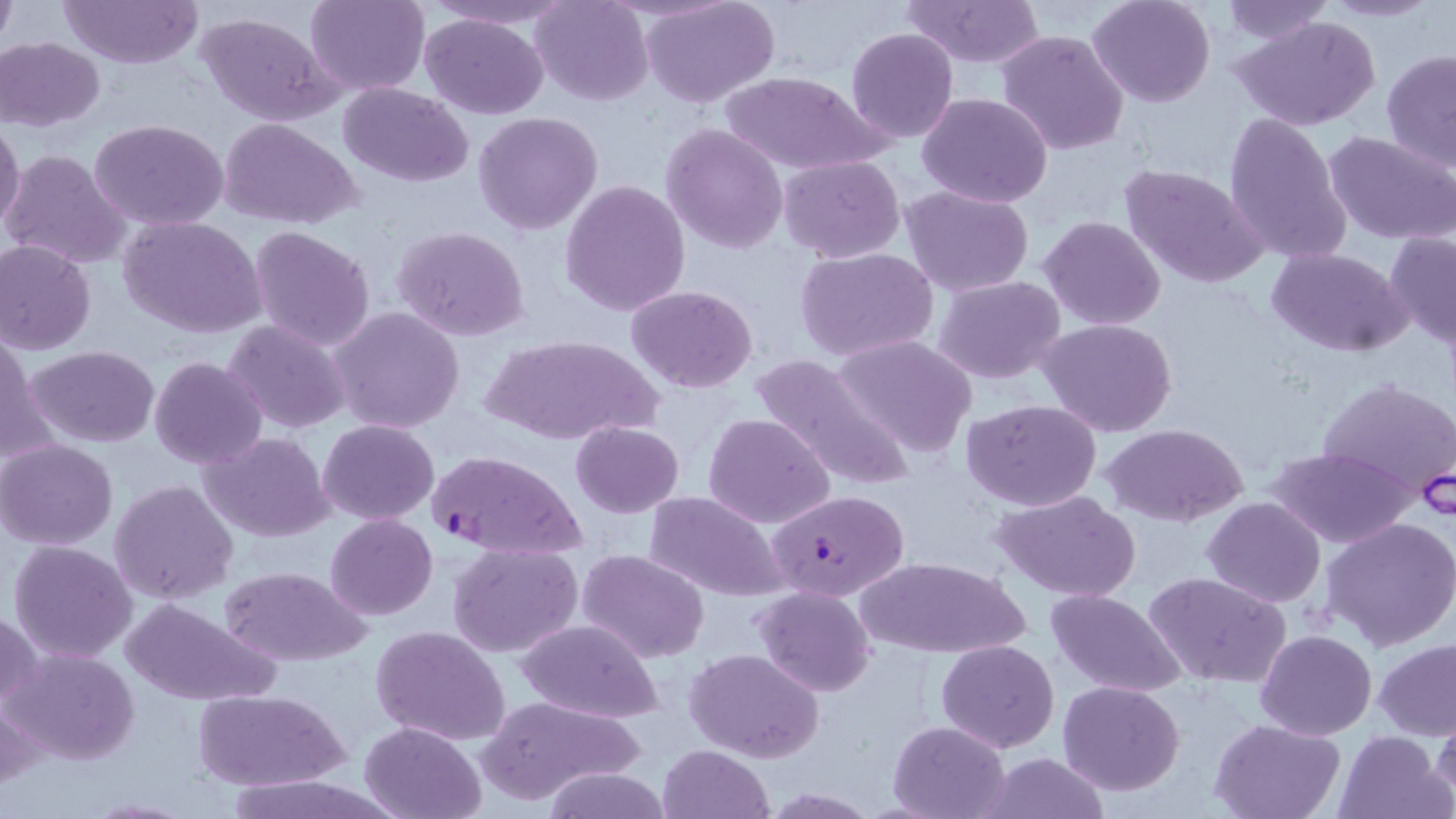 Approximate bounding boxes as (x1,y1)-(x2,y2) corner pairs in pixels. Plasmodium falciparum-infected red blood cell locations: (427,451)-(586,562), (767,487)-(907,604). Uninfected red blood cell locations: (58,0)-(203,70), (306,0)-(430,96), (427,0)-(572,29), (528,0)-(652,107), (645,0)-(780,107), (902,0)-(1045,67), (1087,0)-(1217,108), (1314,0)-(1444,22), (1222,1)-(1333,43), (1,5)-(17,53), (197,12)-(342,127), (418,13)-(550,120), (1236,16)-(1381,132), (846,28)-(960,145), (996,30)-(1128,155), (1,37)-(104,129), (1382,48)-(1456,174), (716,68)-(891,175), (340,82)-(474,185), (918,93)-(1053,208), (1224,111)-(1351,264), (473,112)-(604,236), (89,118)-(230,233), (221,118)-(362,229), (0,119)-(26,231), (660,123)-(789,254), (1326,131)-(1456,243), (2,148)-(131,268), (779,154)-(904,261), (1119,162)-(1267,290), (561,181)-(690,318), (902,185)-(1035,295), (119,215)-(265,338), (1039,215)-(1165,330), (392,225)-(531,342), (249,226)-(376,352), (1384,230)-(1456,348), (0,241)-(97,355), (793,246)-(940,362), (1266,248)-(1411,356), (934,276)-(1066,385), (628,284)-(758,393), (328,306)-(466,434), (221,318)-(351,436), (1037,318)-(1178,438), (481,334)-(659,447), (831,335)-(978,458), (1,338)-(47,465), (28,344)-(159,447), (747,349)-(915,492), (150,357)-(268,471), (1319,378)-(1455,500), (962,399)-(1101,512), (704,412)-(834,528), (318,418)-(438,524), (572,421)-(684,517), (1104,424)-(1247,527), (199,431)-(333,542), (0,439)-(120,549), (1265,446)-(1416,548), (109,480)-(240,604), (996,490)-(1140,600), (644,492)-(788,602), (1202,497)-(1326,606), (325,513)-(438,620), (1324,517)-(1456,651), (8,539)-(138,664), (449,541)-(585,658), (579,549)-(710,661), (854,553)-(1030,658), (222,566)-(370,666), (1145,571)-(1291,687), (752,585)-(875,697), (1045,587)-(1188,698), (122,598)-(276,706), (0,609)-(44,717), (515,618)-(664,722), (371,625)-(511,749), (1257,630)-(1376,739), (1373,638)-(1456,739), (937,640)-(1058,753), (6,647)-(138,765), (683,647)-(825,764), (1057,680)-(1185,795), (194,688)-(347,790), (476,695)-(641,807), (0,697)-(46,792), (1430,709)-(1456,804), (1209,718)-(1347,819), (359,719)-(485,819), (887,719)-(1010,819), (1335,730)-(1452,819), (657,744)-(773,819), (981,754)-(1112,818), (535,768)-(677,819), (221,774)-(395,819), (83,798)-(196,818). Slide-level diagnosis: Plasmodium falciparum. Thin blood film. Captured at 1000x magnification. Image is 1456×819 pixels. One field of a larger specimen. May-Grünwald-Giemsa stain. Optical microscopy.